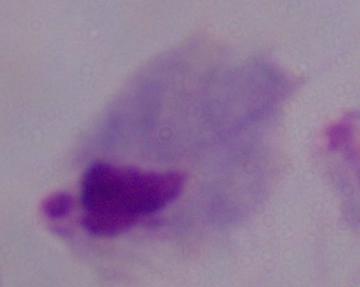
A trichomonad is shown. 1000x magnification. Photomicrograph.